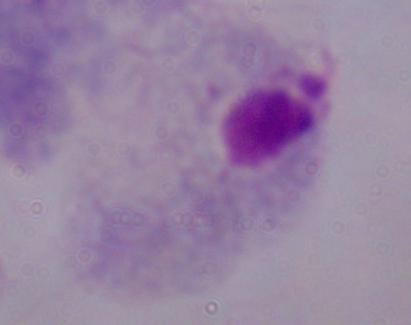
Summary:
  - Magnification: 1000x
  - Identification: trichomonad
  - Modality: photomicrograph